Give the preparation type.
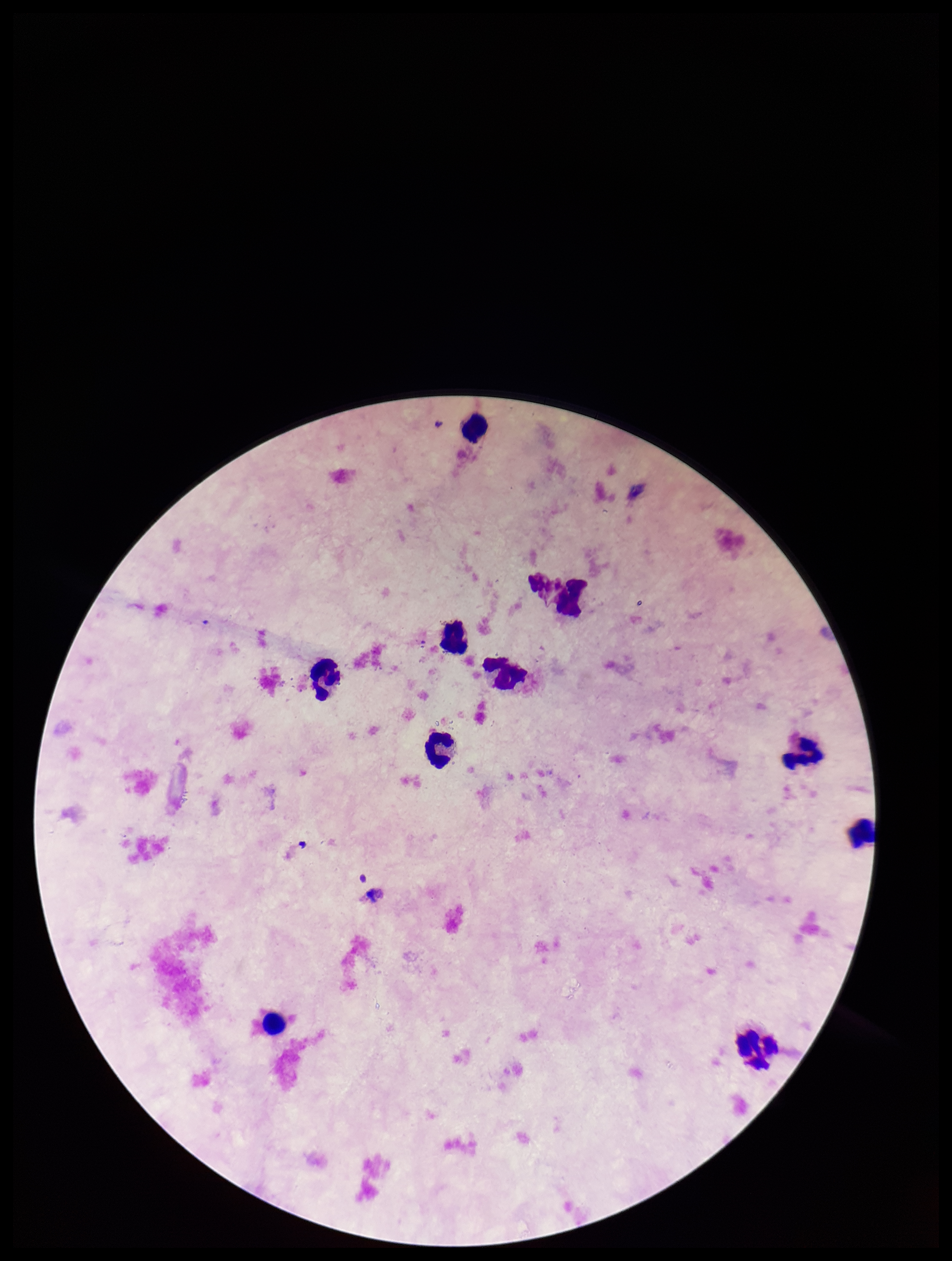
Thick.

One field from this slide. Leukocyte count: 10. Parasite count: 0. Image is 952×1261 pixels. Giemsa stain. Patient malaria status: negative. Smartphone photograph taken through the eyepiece of a microscope. Plasmodium parasites: none detected.